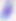
Summary:
  - Identification: Toxoplasma gondii
  - Magnification: 400x
  - Modality: photomicrograph